Identify the cell.
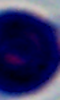
A leukocyte.

Summary:
  - Modality: micrograph
  - Magnification: 1000x